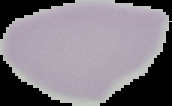
Image is 172×106 pixels. The area outside the segmented cell region is set to black. From a thin blood smear. Malaria status: uninfected.